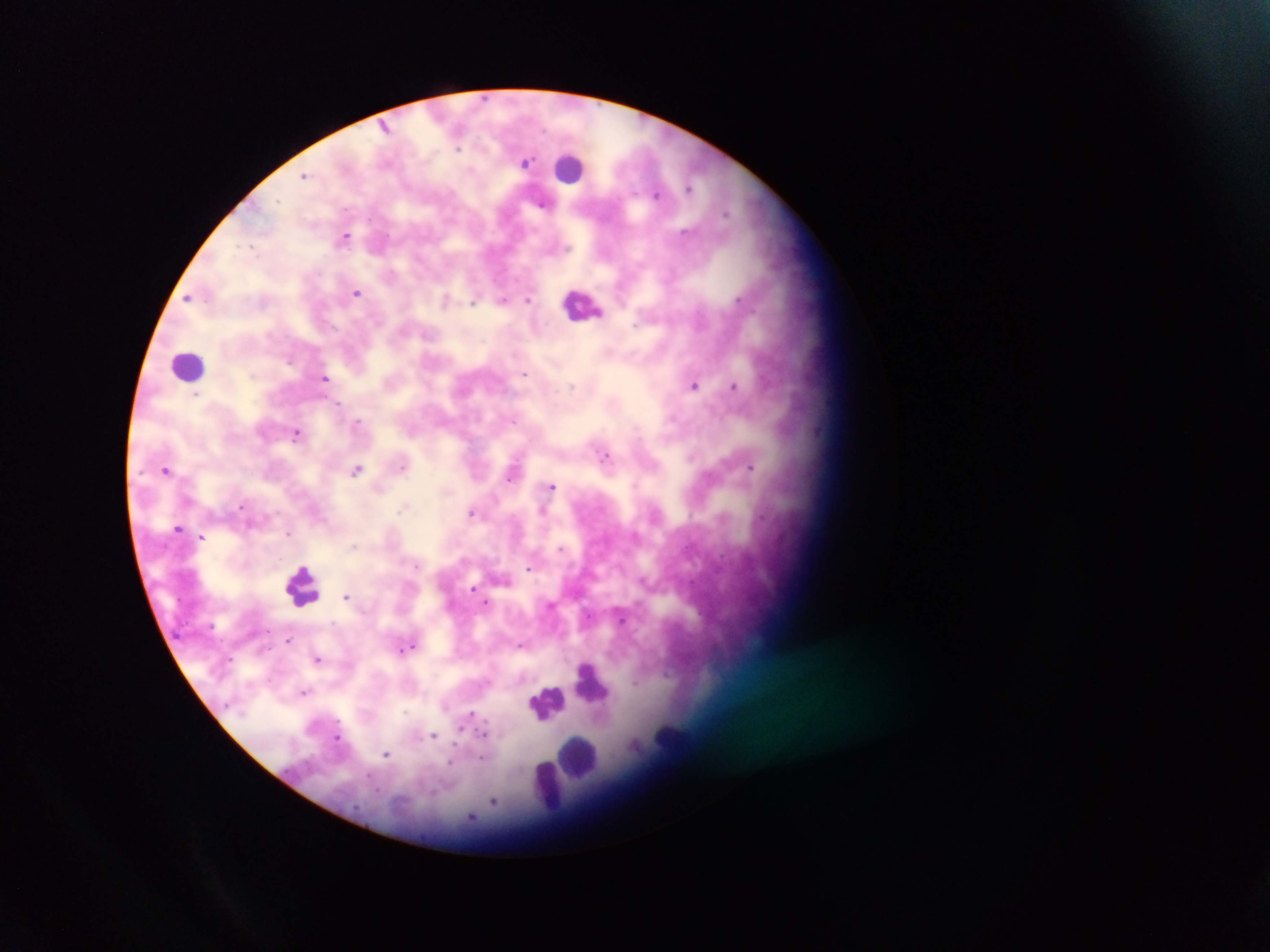
Approximate centers as [x, y] in pixels. Malaria parasite locations: [385, 127], [458, 148], [526, 161], [304, 175], [689, 188], [657, 194], [542, 203], [727, 212], [345, 237], [252, 246], [357, 292], [188, 298], [738, 299], [503, 300], [529, 300], [445, 301], [473, 301], [635, 325], [608, 351], [525, 374], [325, 378], [694, 385], [734, 385], [571, 387], [196, 394], [339, 404], [357, 421], [514, 421], [296, 433], [604, 456], [403, 466], [751, 467], [357, 469], [167, 470], [510, 476], [551, 487], [241, 504], [402, 507], [472, 512], [543, 512], [178, 527], [288, 534], [201, 537], [354, 546], [561, 548], [529, 568], [473, 588], [347, 596], [487, 602], [267, 630], [289, 640], [521, 645], [410, 647], [318, 659], [303, 692], [471, 715], [483, 735], [434, 736], [337, 738], [387, 755], [482, 758], [451, 761], [493, 802]. Leukocyte locations (subset; some below the resolvable size): [572, 169], [582, 304], [189, 365], [303, 585], [592, 681], [547, 701], [670, 743], [578, 755], [548, 788]. Collected in Ghana. Mobile-phone photograph taken through the microscope. Thick blood smear. Image is 1270×952 pixels. One field of view.